Classify this cell by malaria status.
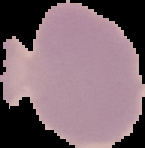
It is uninfected.

From a thin blood smear. Cell region segmented out of the field of view; the surrounding area is masked to black. Image is 145×148 pixels.